Classify this cell by malaria status.
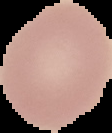
It is uninfected.

From a thin blood smear. Image is 112×133 pixels. Segmented cell region on a black background.